Outline each uninfected red blood cell.
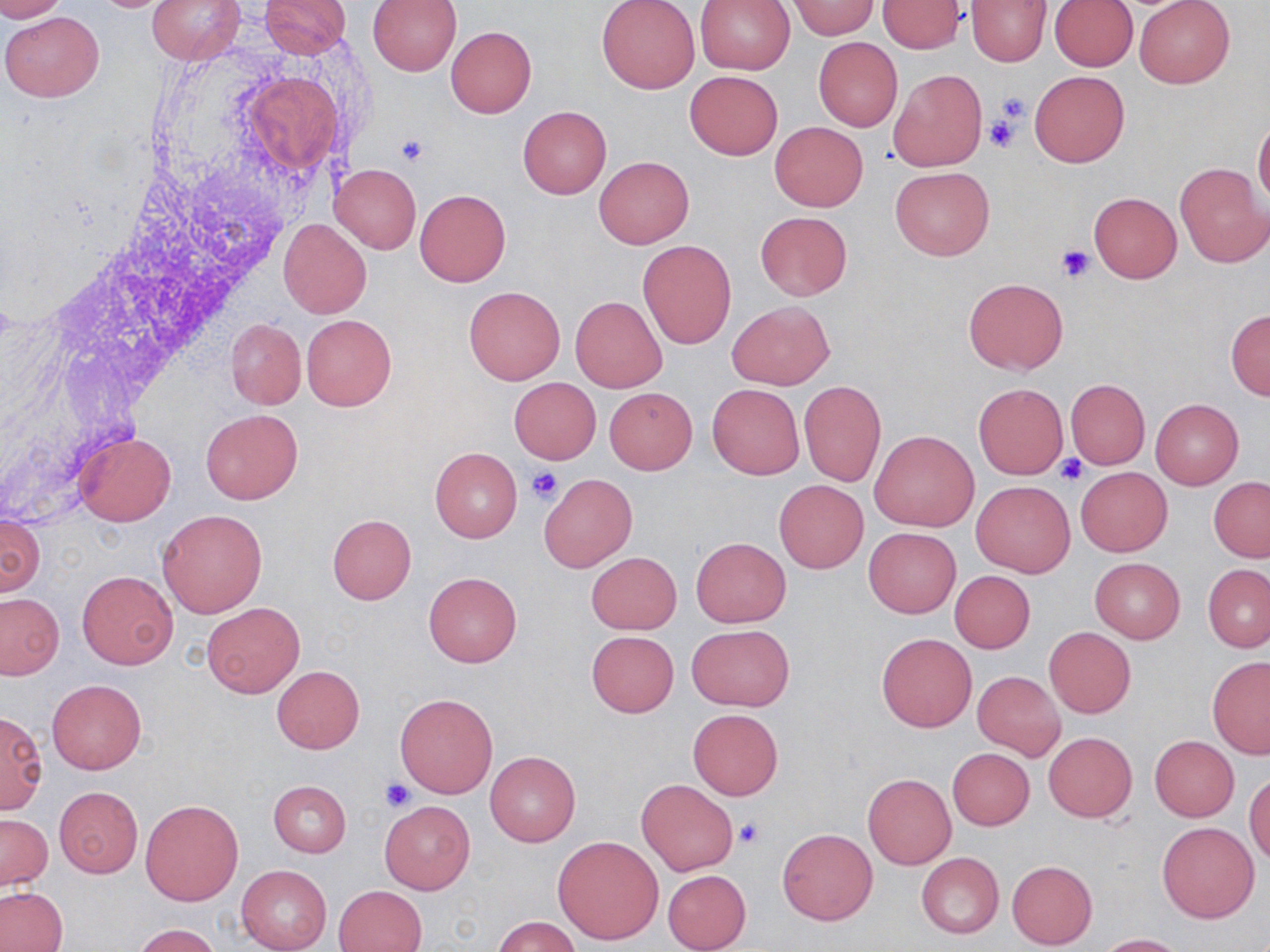

Approximate bounding boxes as (x1,y1)-(x2,y2) corner pairs in pixels.
Uninfected red blood cells: (0,0)-(70,21), (147,0)-(245,64), (260,0)-(352,56), (368,0)-(461,75), (596,0)-(700,95), (965,0)-(1051,67), (695,1)-(795,74), (877,1)-(966,53), (1050,1)-(1137,70), (1134,1)-(1234,88), (789,2)-(878,38), (1,10)-(104,103), (446,26)-(537,119), (813,38)-(903,132), (888,69)-(986,171), (685,71)-(782,159), (1029,71)-(1129,168), (517,105)-(613,199), (1253,117)-(1270,210), (769,121)-(868,211), (593,156)-(694,249), (1175,162)-(1270,268), (331,164)-(421,254), (889,166)-(994,261), (415,189)-(510,287), (1089,192)-(1180,282), (755,211)-(851,301), (278,219)-(371,318), (638,240)-(736,348), (963,277)-(1069,376), (463,286)-(565,385), (570,296)-(666,392), (726,300)-(834,389), (1225,309)-(1269,400), (301,314)-(396,411), (225,318)-(305,409), (508,377)-(601,464), (1065,379)-(1149,469), (799,380)-(886,488), (973,383)-(1067,478), (707,384)-(804,479), (604,387)-(697,474), (1149,399)-(1243,490), (200,409)-(302,504), (870,429)-(980,531), (73,430)-(176,526), (430,447)-(522,543), (1076,467)-(1171,556), (539,474)-(637,573), (1209,477)-(1270,561), (970,479)-(1075,578), (774,480)-(868,573), (157,508)-(269,618), (0,512)-(44,598), (327,513)-(415,604), (863,527)-(960,618), (690,536)-(791,628), (585,552)-(682,634), (1089,558)-(1185,643), (1203,564)-(1270,652), (949,570)-(1035,653), (77,571)-(178,669), (424,572)-(521,667), (0,594)-(62,678), (202,602)-(304,698), (686,625)-(794,710), (1044,627)-(1136,718), (586,630)-(679,717), (876,633)-(976,732), (1207,657)-(1270,759), (272,665)-(364,753), (973,671)-(1065,760), (47,679)-(146,773), (395,693)-(498,798), (0,709)-(47,814), (687,709)-(783,800), (1043,732)-(1137,822), (1149,735)-(1239,821), (947,748)-(1033,830), (485,751)-(580,846), (863,774)-(956,870), (1244,774)-(1270,866), (637,779)-(739,875), (267,780)-(351,857), (53,786)-(143,878), (139,799)-(243,906), (379,800)-(475,894), (1,814)-(52,891), (1157,822)-(1259,923), (777,828)-(877,926), (553,836)-(664,944), (915,851)-(1004,939), (1006,860)-(1097,949), (237,865)-(331,952), (662,869)-(751,951), (334,884)-(427,952), (1,887)-(67,952), (495,916)-(581,952), (133,924)-(221,952), (1097,933)-(1185,951).

Summary:
  - Platelet locations: (992,91)-(1030,136), (984,113)-(1022,154), (395,134)-(431,166), (1056,243)-(1097,282), (1056,455)-(1088,486), (525,466)-(562,504), (380,776)-(417,812), (735,819)-(765,849)
  - Slide-level diagnosis: no evidence of blood parasites
  - Modality: optical microscopy
  - Stain: May-Grünwald-Giemsa
  - Image size: 1270×952 pixels
  - Preparation: thin blood film
  - Magnification: 1000x
  - Field of view: one of a larger specimen